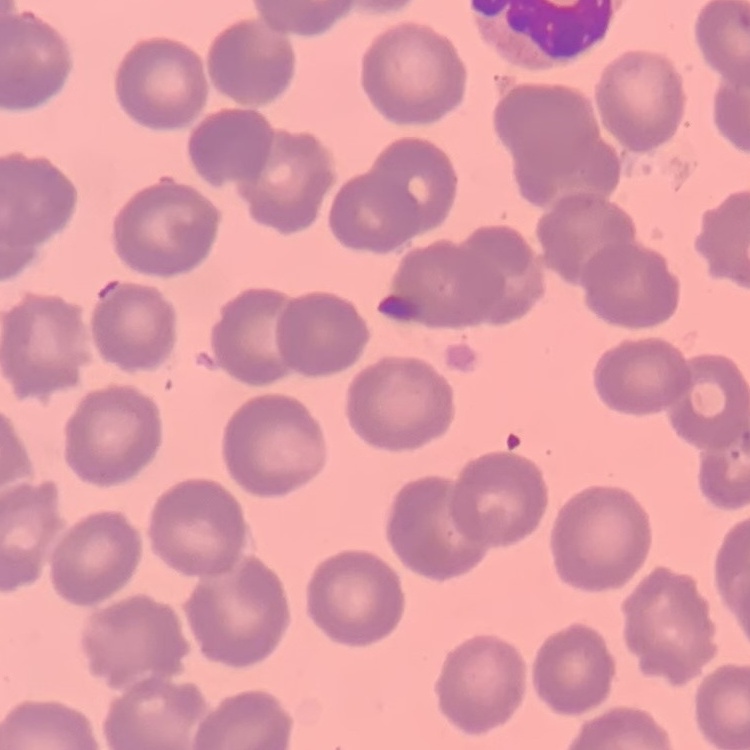

erythrocyte morphology = no rouleaux formation
preparation = thin peripheral smear
stain = Field's or Giemsa
image type = one tile cut from a larger photomicrograph